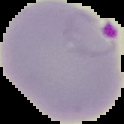
Summary:
  - Image type: segmented cell region with the area outside set to black
  - Preparation: thin blood film
  - Result: malaria parasites detected
  - Image size: 124×124 pixels